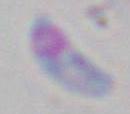

Summary:
  - Magnification: 1000x
  - Modality: micrograph
  - Identification: Toxoplasma gondii